Classify this cell by malaria status.
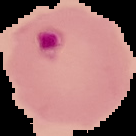

Parasitized.

Summary:
  - Image type: segmented cell region with the area outside set to black
  - Preparation: thin blood smear
  - Image size: 136×136 pixels